Classify this cell by malaria status.
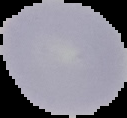

It is uninfected.

{
  "image_type": "segmented cell region on a black background",
  "preparation": "thin blood smear",
  "image_size": "127×118 pixels"
}